Classify this cell by malaria status.
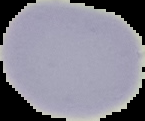

It is uninfected.

Summary:
  - Image type: segmented cell region with the area outside set to black
  - Preparation: thin blood film
  - Image size: 145×121 pixels